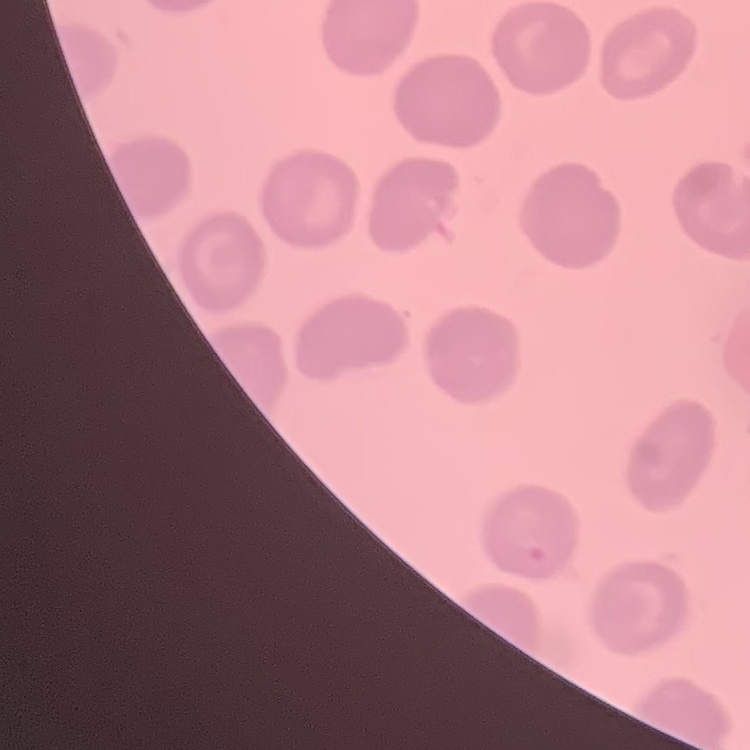

The erythrocytes exhibit no rouleaux formation. Stained with either Field's or Giemsa. Thin blood smear. Square crop of a larger photomicrograph.